Locate leukocytes (white blood cells).
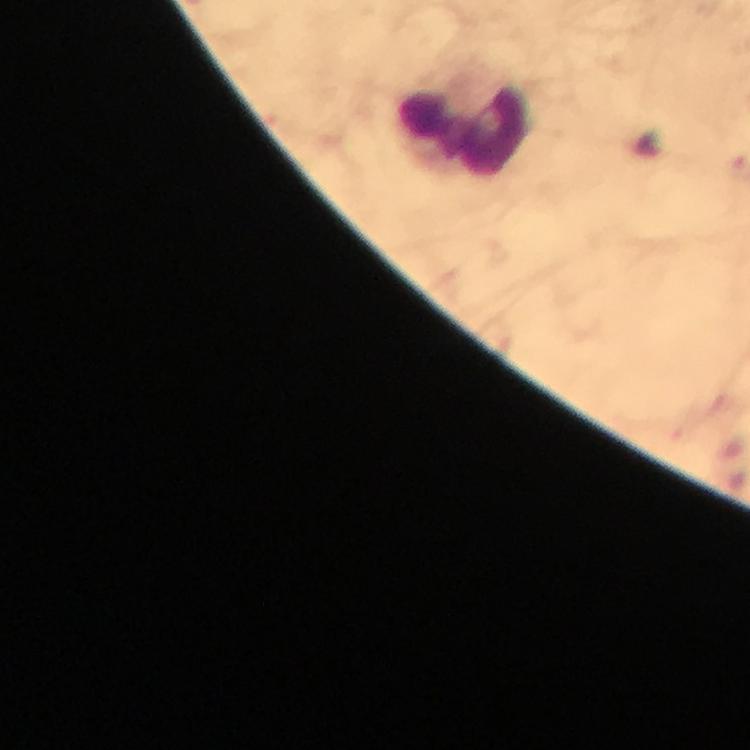
Approximate centers as {x, y} in pixels.
Leukocytes: {464, 127}.

{
  "magnification": "100x",
  "cropped_from": "a single field of view",
  "immersion_oil": "applied",
  "image_size": "750×750 pixels",
  "malaria_parasites": "none seen",
  "stain": "Giemsa",
  "preparation": "thick smear",
  "context": "from a diagnostic examination for malaria",
  "capture": "smartphone camera through the microscope"
}